Identify the parasite.
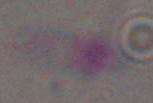

Toxoplasma gondii.

modality = micrograph
magnification = 1000x